Identify the parasite.
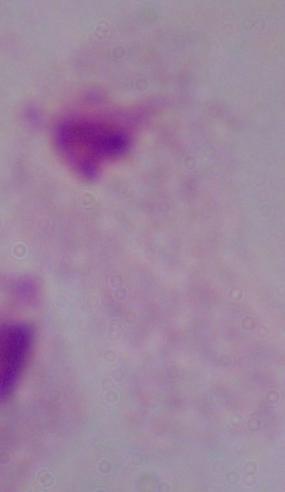
A trichomonad.

Captured at 1000x magnification. Micrograph.